Classify this cell by malaria status.
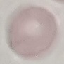

It is uninfected.

Summary:
  - Preparation: thin blood smear
  - Image type: cell patch, automatically extracted from a larger field of view and resized to 64 × 64 pixels
  - Stain: Giemsa
  - Capture: smartphone camera at the microscope eyepiece